Classify this cell by malaria status.
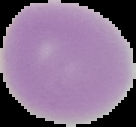

It is uninfected.

image size = 136×127 pixels
preparation = thin blood film
image type = segmented cell region on a black background